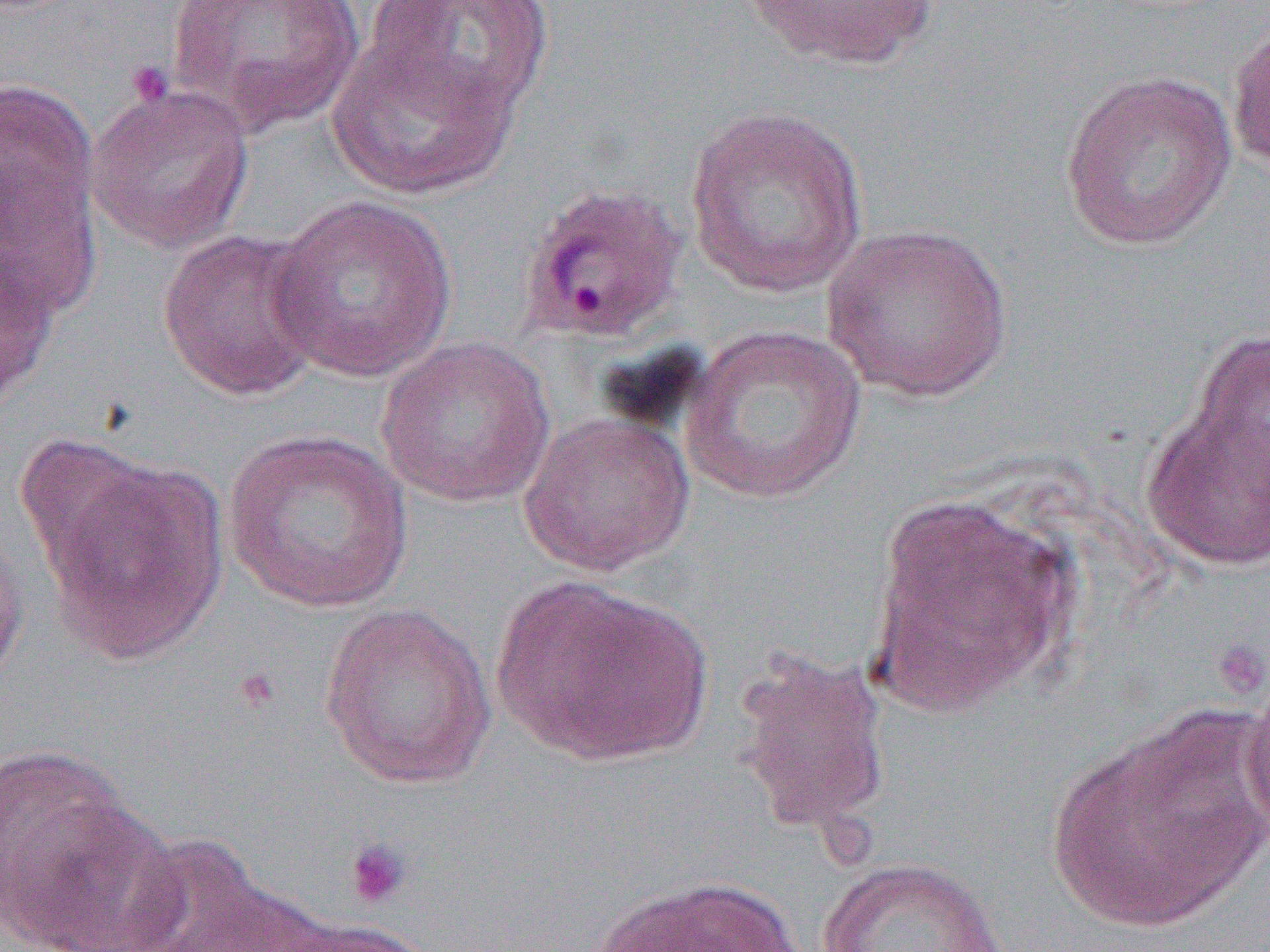
slide_level_diagnosis: Plasmodium ovale
platelet_locations: 'approximate bounding boxes as (x1, y1, x2, y2) in pixels: (125, 60, 176, 108), (1211, 636, 1270, 702), (232, 666, 282, 714), (343, 837, 411, 909)'
uninfected_red_blood_cell_locations: 'approximate bounding boxes as (x1, y1, x2, y2) in pixels: (166, 0, 365, 135), (364, 0, 556, 122), (741, 0, 939, 72), (1227, 19, 1270, 177), (326, 32, 519, 202), (1059, 69, 1237, 252), (0, 74, 101, 283), (85, 84, 256, 254), (683, 105, 870, 299), (267, 195, 458, 384), (821, 223, 1013, 402), (156, 228, 329, 402), (0, 249, 60, 412), (680, 324, 867, 505), (1183, 324, 1270, 509), (376, 335, 555, 508), (1140, 388, 1270, 574), (518, 413, 695, 577), (223, 428, 415, 613), (37, 451, 229, 665), (867, 489, 1082, 717), (0, 517, 29, 691), (491, 574, 713, 767), (319, 602, 496, 789), (732, 653, 892, 835), (1241, 666, 1270, 845), (1044, 709, 1266, 934), (0, 746, 154, 944), (118, 835, 286, 951), (816, 857, 1012, 952), (589, 876, 804, 952), (270, 918, 441, 952)'
field_of_view: one of a larger specimen
modality: optical microscopy
preparation: thin blood smear
image_size: 1270×952 pixels
magnification: 1000x